Classify this cell by malaria status.
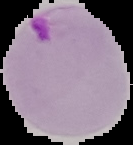
It is parasitized.

Image is 133×145 pixels. The area outside the segmented cell region is set to black. From a thin blood smear.